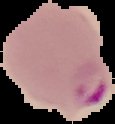

image type = segmented cell region with the area outside set to black
result = malaria parasites detected
image size = 115×124 pixels
preparation = thin blood film